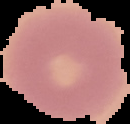 Image is 130×124 pixels. From a thin blood smear. Malaria status: uninfected. Segmented cell region on a black background.